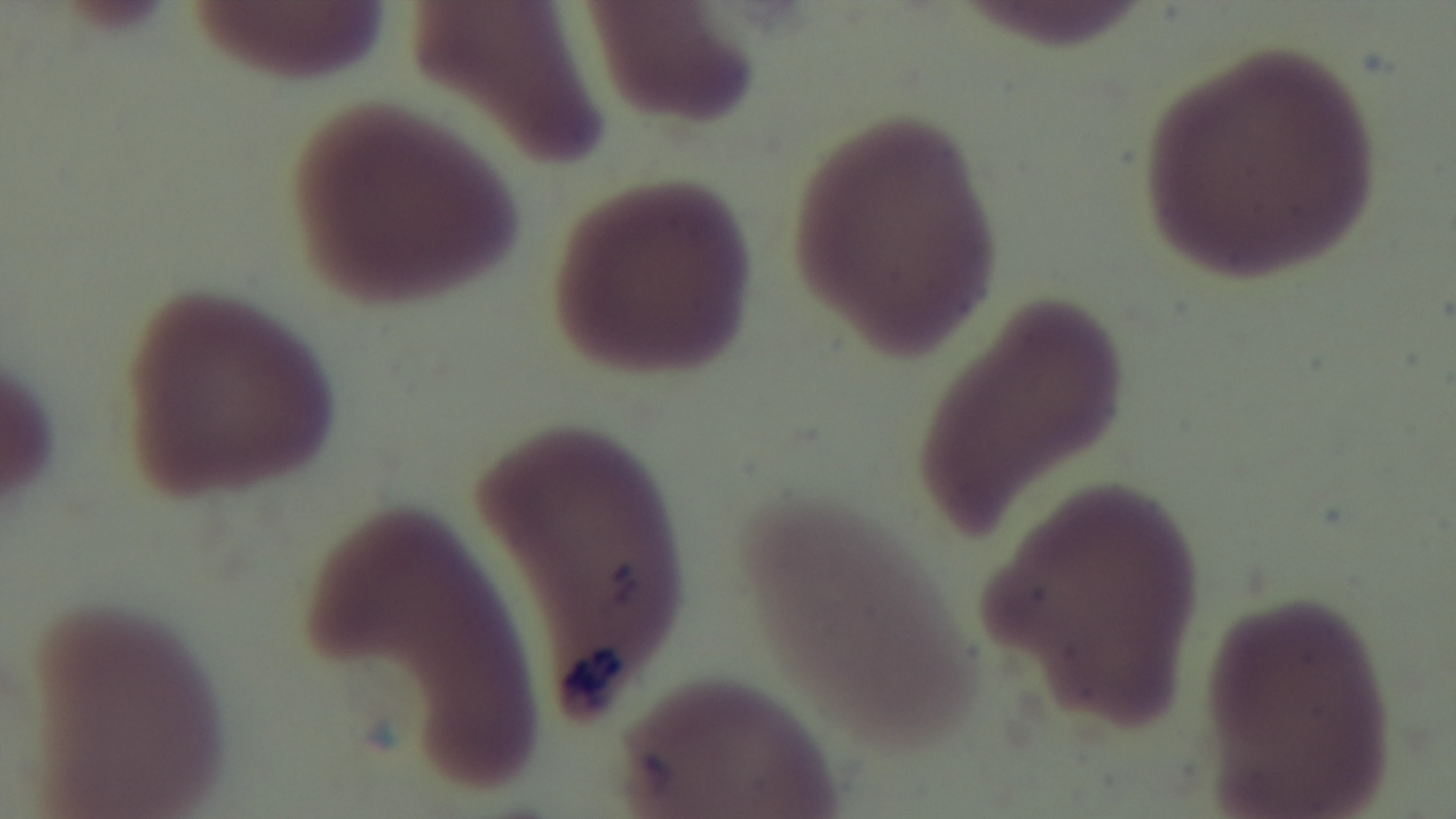
{
  "preparation": "thin",
  "field_of_view": "single",
  "objective": "100x oil immersion",
  "stain": "Giemsa",
  "capture": "mounted 4K digital camera",
  "modality": "light microscopy",
  "malaria_status": "uninfected"
}